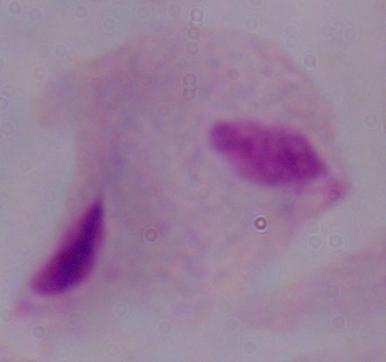
A trichomonad is shown. Photomicrograph. 1000x magnification.